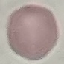
result: negative for malaria parasites
stain: Giemsa
preparation: thin blood film
capture: smartphone through the microscope eyepiece
image_type: automatically extracted cell patch, resized to 64 × 64 pixels